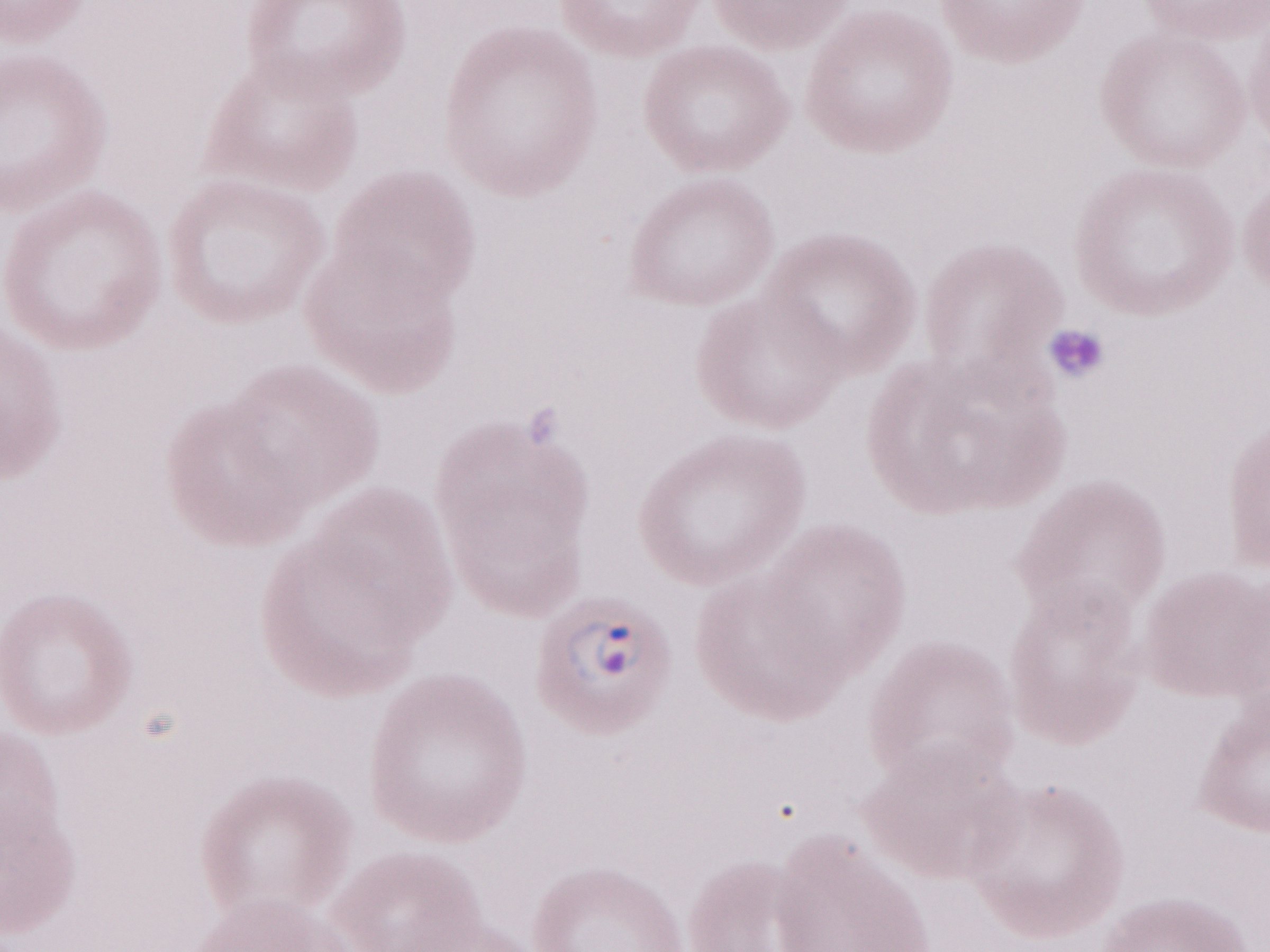 Patient-level malaria diagnosis: positive. Image is 1270×952 pixels. Magnification: 1,000x. One field of this slide. Thin peripheral-blood smear. May-Grünwald-Giemsa stain. Olympus BX43 microscope, Olympus DP73 camera.